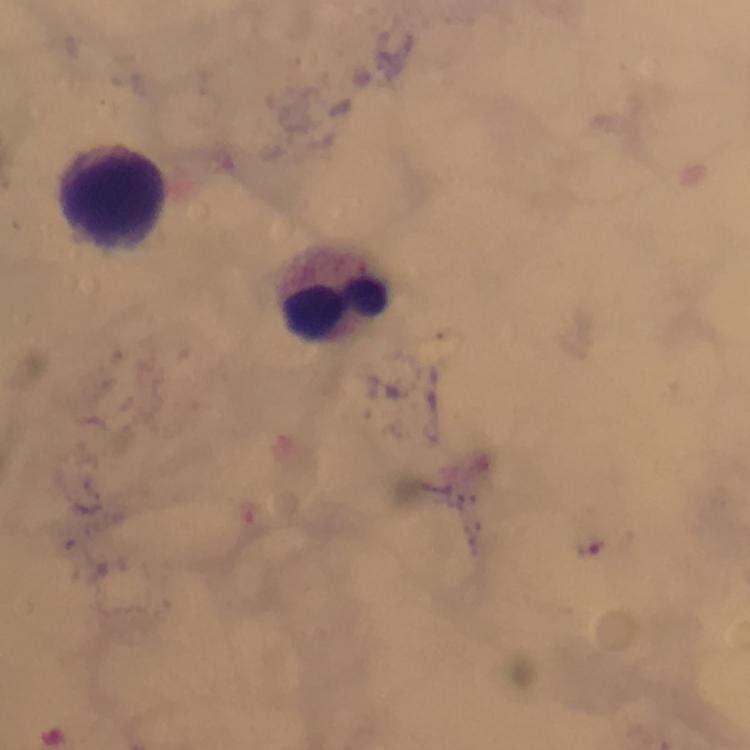
Approximate object centers, in pixels from the top-left corner. Leukocyte locations: (x=113, y=194), (x=334, y=294). Malaria parasite locations: (x=590, y=547). From a malaria diagnostic workup. Image is 750×750 pixels. Thick blood smear. Giemsa stain. Cropped region of a single field of view. At 100x magnification. Immersion oil was used. Photographed with a smartphone mounted on the microscope.